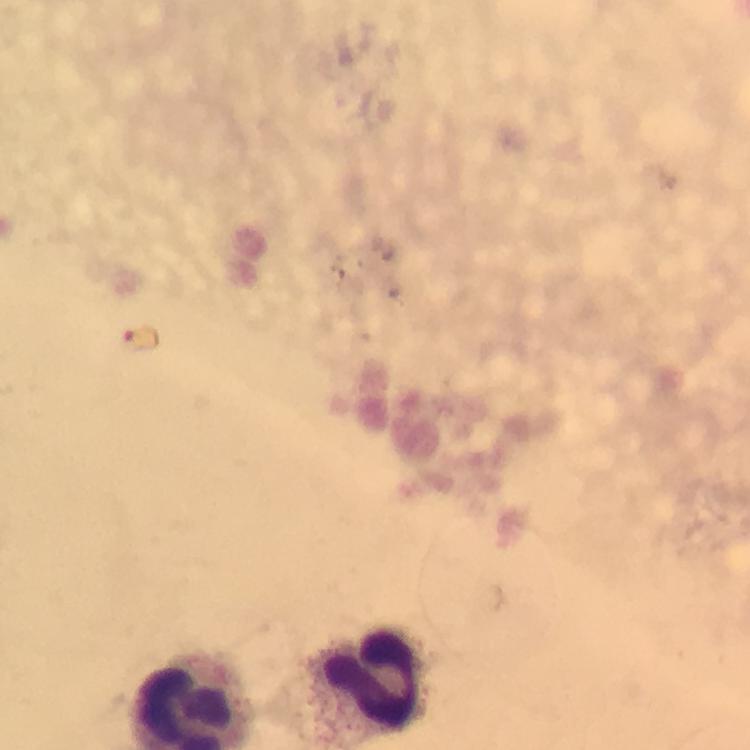
Approximate centers as [x, y] in pixels.
Summary:
  - Leukocyte locations: [370, 683]
  - Stain: Giemsa
  - Image size: 750×750 pixels
  - Context: from a malaria diagnostic workup
  - Preparation: thick smear
  - Malaria parasites: none detected
  - Cropped from: a single field of view
  - Capture: smartphone mounted on the microscope
  - Immersion oil: applied
  - Magnification: 100x